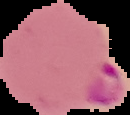
preparation = thin blood film
malaria status = parasitized
image type = segmented cell region with the area outside set to black
image size = 130×115 pixels